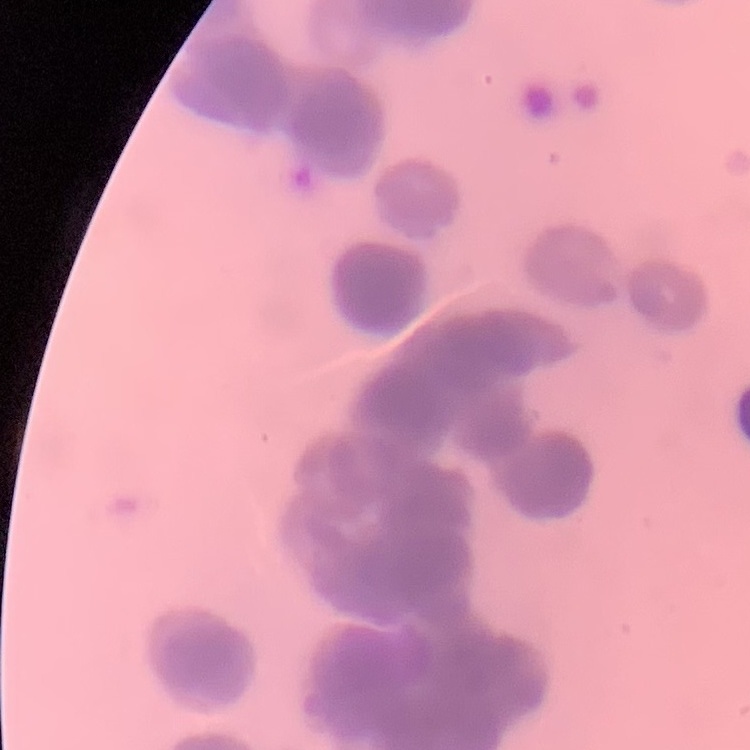
Summary:
  - Red blood cell morphology: rouleaux formation
  - Image type: square crop of a larger photomicrograph
  - Stain: Field's or Giemsa
  - Preparation: thin peripheral smear